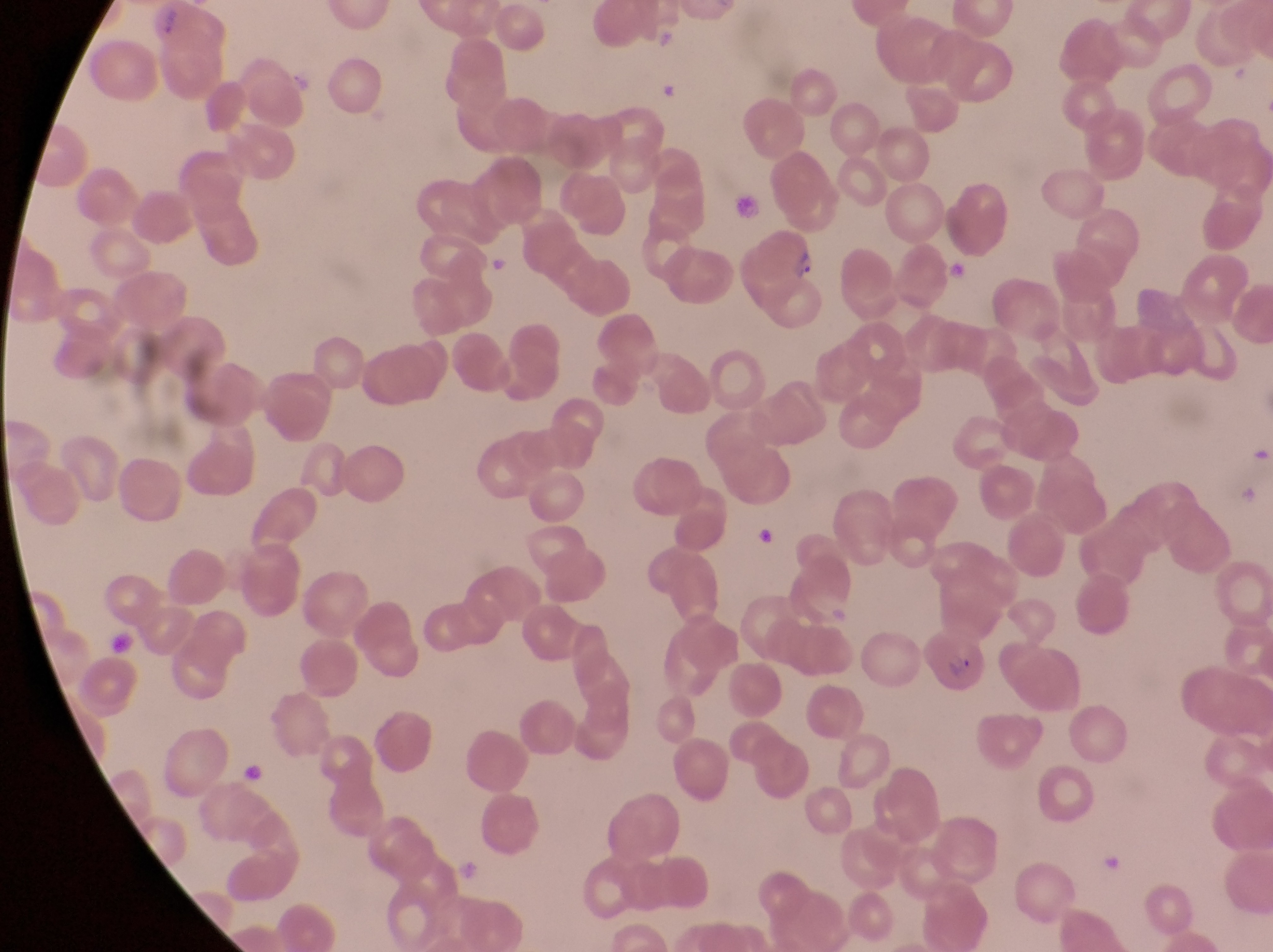

parasitised_red_blood_cell_locations: 'approximate bounding boxes as {left, top, right, bottom} in pixels: {746, 227, 816, 322}, {923, 622, 986, 694}'
image_size: 1273×952 pixels
artifact_platelet_like_body_stain_precipitate_or_debris_locations: 'approximate bounding boxes as {left, top, right, bottom} in pixels: {941, 259, 973, 287}, {239, 767, 272, 790}'
field_of_view: single
capture: smartphone photograph through the eyepiece of an Olympus CX-23 microscope
preparation: thin blood film
country: Uganda
magnification: 1000x